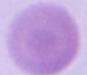
Summary:
  - Identification: erythrocyte
  - Modality: photomicrograph
  - Magnification: 1000x